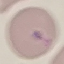
Malaria status: uninfected. Photographed with a smartphone camera at the microscope eyepiece. Giemsa stain. Thin blood film. Automatically extracted cell patch, resized to 64 × 64 pixels.